Comment on the morphology of the red blood cells.
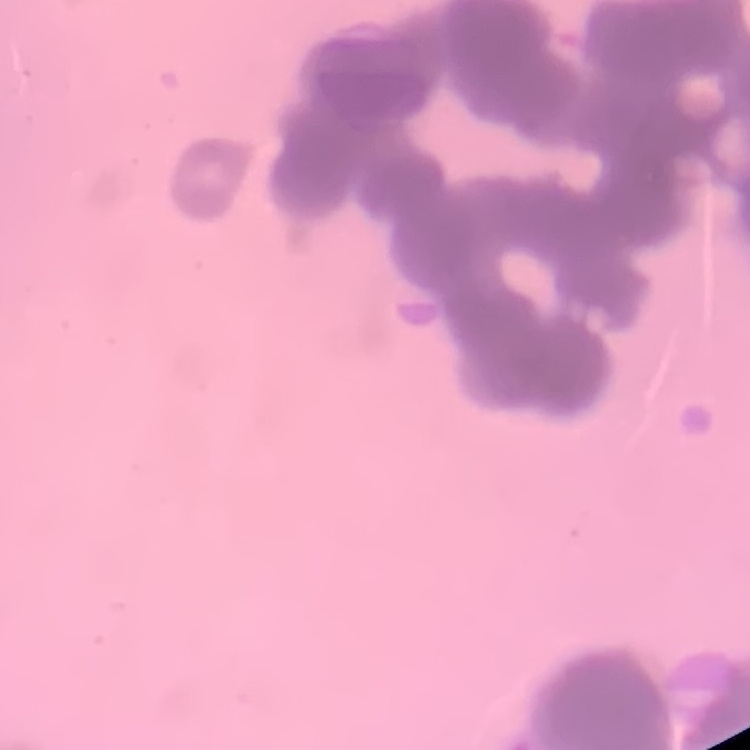
Rouleaux formation.

Summary:
  - Stain: Field's or Giemsa
  - Preparation: thin peripheral smear
  - Image type: one tile cut from a larger photomicrograph